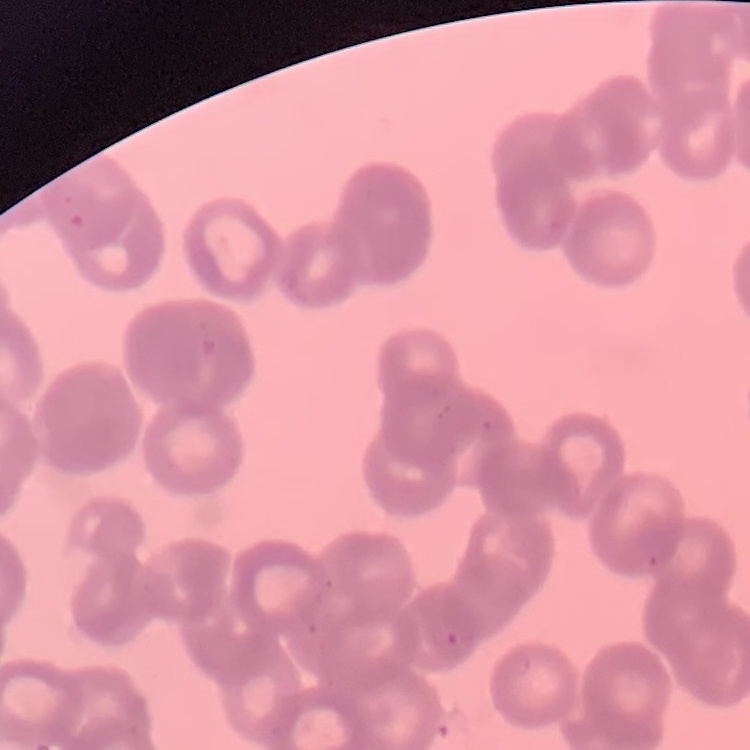
Summary:
  - Red blood cell morphology: rouleaux formation
  - Image type: square crop of a larger photomicrograph
  - Stain: Field's or Giemsa
  - Preparation: thin blood smear